State which cell type is depicted.
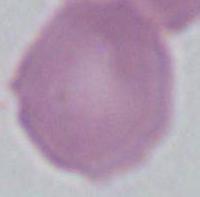

This is an erythrocyte.

Micrograph. 1000x magnification.